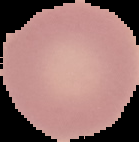
malaria_status: uninfected
image_size: 139×142 pixels
preparation: thin blood smear
image_type: segmented cell region on a black background